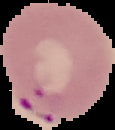

Summary:
  - Malaria status: parasitized
  - Preparation: thin blood film
  - Image type: segmented cell region with the area outside set to black
  - Image size: 115×130 pixels